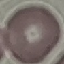
result: negative for malaria parasites
image_type: cell patch, automatically extracted from a larger field of view and resized to 64 × 64 pixels
stain: Giemsa
preparation: thin blood smear
capture: smartphone camera at the microscope eyepiece